Classify this cell by malaria status.
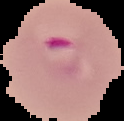
It is parasitized.

Image is 124×121 pixels. From a thin blood film. Segmented cell region on a black background.